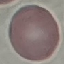

{
  "result": "no malaria parasites detected",
  "stain": "Giemsa",
  "capture": "smartphone through the microscope eyepiece",
  "preparation": "thin smear",
  "image_type": "automatically extracted cell patch, resized to 64 × 64 pixels"
}